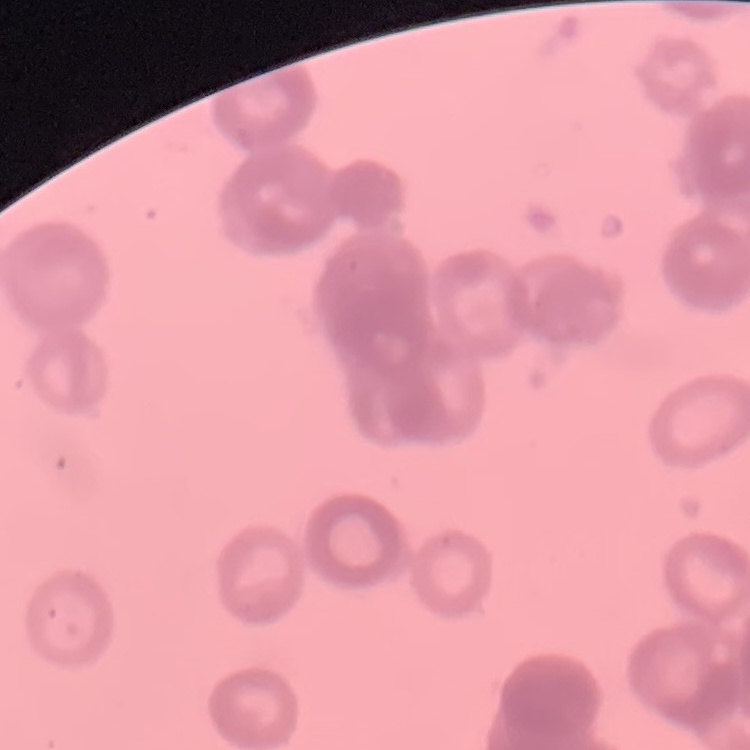
Summary:
  - Red blood cell morphology: rouleaux formation
  - Stain: Field's or Giemsa
  - Image type: one tile cut from a larger photomicrograph
  - Preparation: thin blood film